State which parasite is depicted.
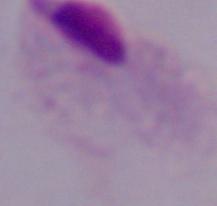
A trichomonad.

Micrograph. 1000x magnification.